Mark where leukocytes are.
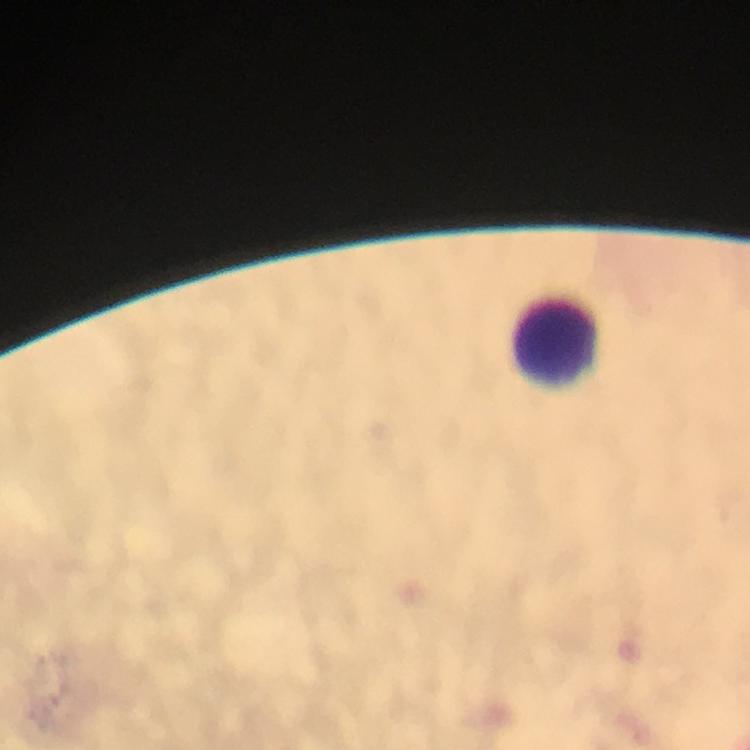
Approximate centers as [x, y] in pixels.
Leukocytes: [555, 340].

Summary:
  - Image size: 750×750 pixels
  - Magnification: 100x
  - Malaria parasites: none detected
  - Context: from a diagnostic examination for malaria
  - Stain: Giemsa
  - Preparation: thick blood film
  - Cropped from: a single field of view
  - Capture: smartphone mounted on the microscope
  - Immersion oil: used